Identify the parasite.
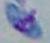

Toxoplasma gondii.

magnification = 1000x
modality = photomicrograph